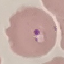
Summary:
  - Malaria status: parasitized
  - Image type: cell patch, automatically extracted from a larger field of view and resized to 64 × 64 pixels
  - Stain: Giemsa
  - Capture: smartphone camera at the microscope eyepiece
  - Preparation: thin smear